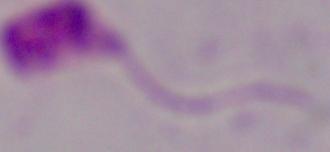
modality = photomicrograph
identification = Leishmania
magnification = 1000x